Assess this cell for malaria.
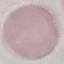

Uninfected.

Cell patch, automatically extracted from a larger field of view and resized to 64 × 64 pixels. Thin blood smear. Giemsa stain. Acquired by smartphone through the microscope eyepiece.